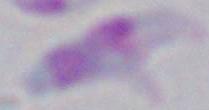

Summary:
  - Modality: micrograph
  - Identification: Toxoplasma gondii
  - Magnification: 1000x